Locate every malaria parasite.
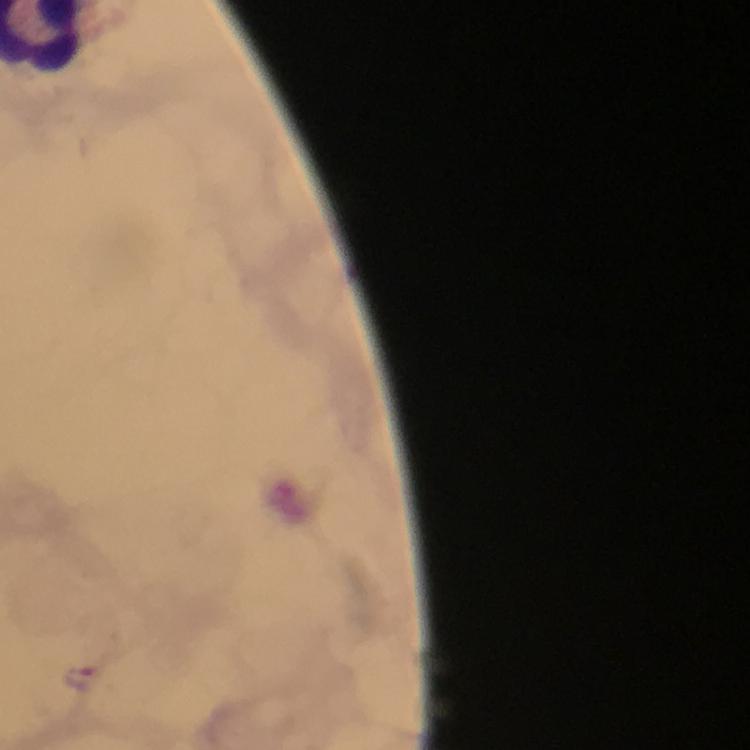

Approximate object centers, in pixels from the top-left corner.
Malaria parasites: (x=81, y=675).

{
  "preparation": "thick blood smear",
  "capture": "smartphone camera through the microscope",
  "stain": "Giemsa",
  "immersion_oil": "applied",
  "context": "from a malaria diagnostic workup",
  "image_size": "750×750 pixels",
  "cropped_from": "one field of view",
  "magnification": "100x"
}